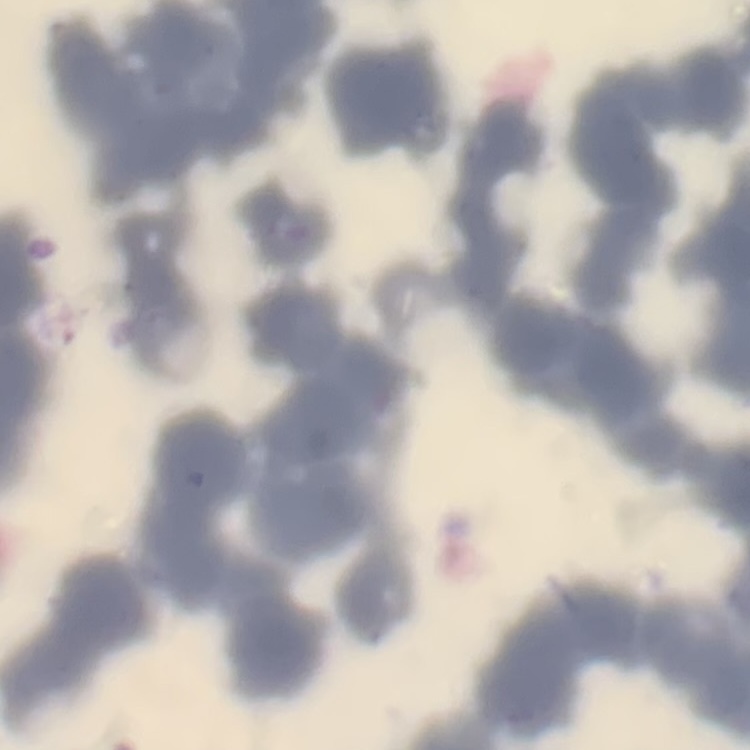
erythrocyte morphology = rouleaux formation
image type = square crop of a larger photomicrograph
preparation = thin blood smear
stain = Field's or Giemsa